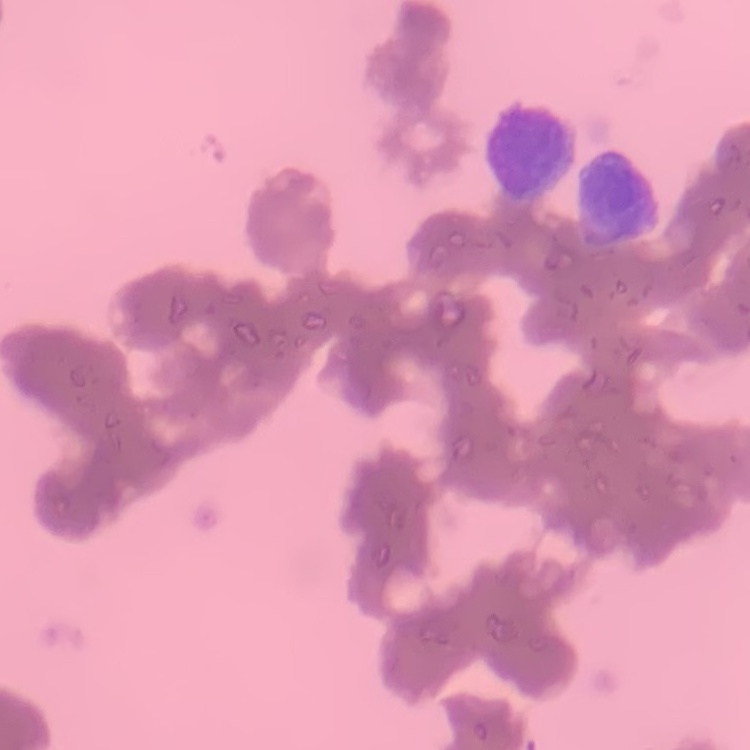 The red blood cells exhibit rouleaux formation. Thin blood film. Stained with either Field's or Giemsa. Square crop of a larger photomicrograph.